Name the cell type shown.
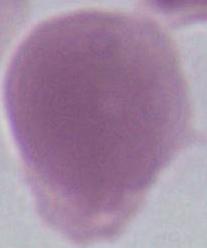

This is an erythrocyte.

Summary:
  - Magnification: 1000x
  - Modality: micrograph